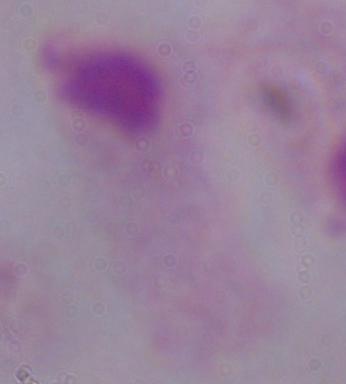

modality = photomicrograph
identification = trichomonad
magnification = 1000x